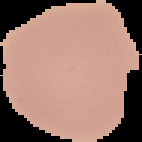
{
  "image_type": "cell region segmented out of the field of view; surrounding area masked to black",
  "preparation": "thin blood film",
  "image_size": "142×142 pixels",
  "malaria_status": "uninfected"
}